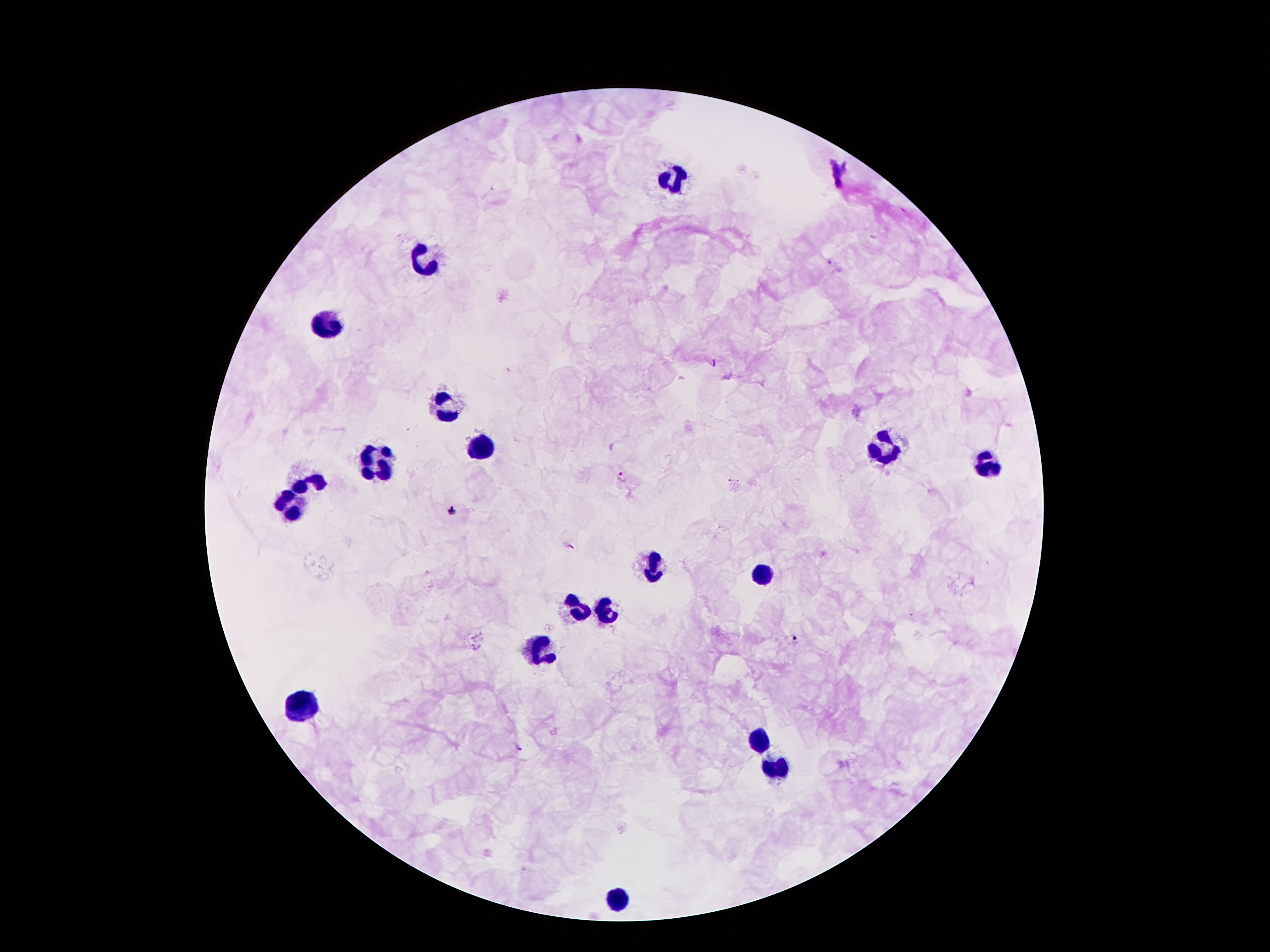

coordinate format = approximate centers as [x, y] in pixels
malaria parasite locations = [829, 262], [622, 475], [453, 513], [795, 636], [516, 747]
leukocyte locations = [670, 180], [425, 255], [327, 321], [444, 409], [884, 447], [486, 449], [376, 463], [985, 465], [311, 479], [288, 503], [652, 565], [763, 575], [577, 607], [609, 610], [539, 649], [302, 703], [757, 741], [777, 766], [617, 899]
magnification = 100x
capture = smartphone camera through the microscope eyepiece
image size = 1270×952 pixels
stain = Giemsa
field of view = single
preparation = thick blood smear
patient malaria status = infected with Plasmodium falciparum